Assess this cell for malaria.
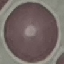
It is uninfected.

Summary:
  - Stain: Giemsa
  - Capture: smartphone through the microscope eyepiece
  - Preparation: thin blood smear
  - Image type: automatically extracted cell patch, resized to 64 × 64 pixels